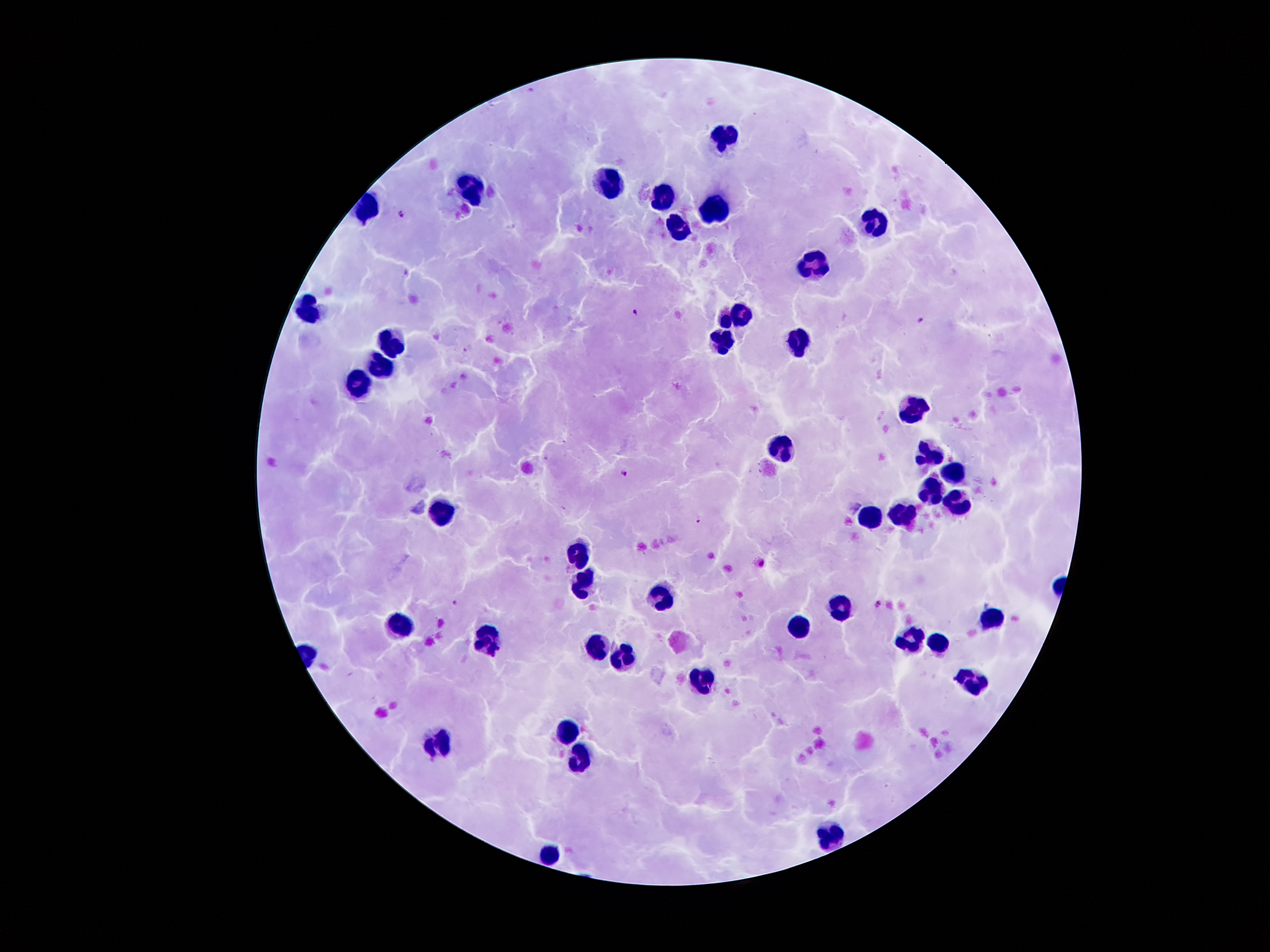
{
  "leukocyte_locations": "approximate centers as {x, y} in pixels: {724, 133}, {614, 185}, {470, 188}, {662, 196}, {368, 204}, {717, 207}, {877, 223}, {677, 227}, {813, 266}, {304, 308}, {742, 314}, {724, 320}, {393, 338}, {726, 342}, {800, 343}, {382, 365}, {357, 386}, {912, 406}, {782, 448}, {931, 452}, {954, 473}, {933, 489}, {959, 501}, {902, 513}, {446, 514}, {868, 517}, {579, 548}, {583, 585}, {663, 597}, {842, 606}, {991, 616}, {401, 625}, {798, 627}, {489, 635}, {910, 637}, {938, 639}, {597, 646}, {624, 657}, {705, 676}, {975, 682}, {567, 732}, {439, 740}, {583, 753}, {835, 836}, {550, 854}",
  "stain": "Giemsa",
  "magnification": "100x",
  "patient_malaria_status": "infected with Plasmodium falciparum",
  "preparation": "thick blood smear",
  "capture": "smartphone through the microscope eyepiece",
  "field_of_view": "one from this slide",
  "plasmodium_parasite_locations": "approximate centers as {x, y} in pixels: {399, 214}, {635, 310}, {921, 320}, {623, 473}, {698, 520}, {878, 603}, {456, 604}",
  "image_size": "1270×952 pixels"
}